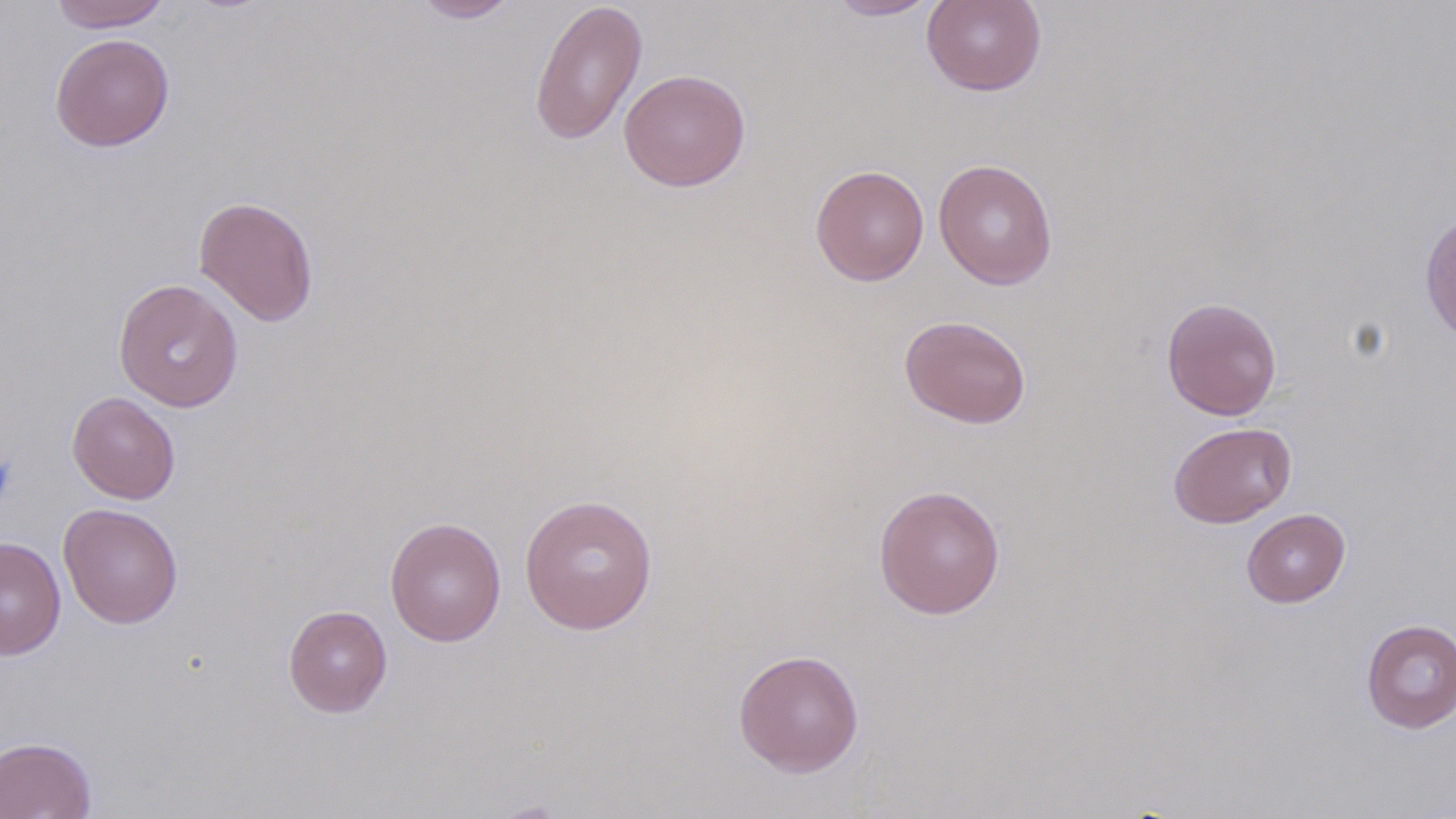 Approximate bounding boxes as [x1, y1, x2, y2] in pixels. Platelet locations: [0, 452, 18, 507]. Uninfected red blood cell locations: [49, 0, 172, 32], [409, 0, 521, 23], [824, 0, 943, 21], [921, 0, 1047, 96], [529, 1, 648, 146], [49, 33, 175, 152], [618, 68, 751, 191], [933, 158, 1058, 289], [810, 165, 930, 286], [193, 195, 320, 327], [113, 279, 244, 412], [1161, 296, 1283, 421], [899, 315, 1031, 429], [67, 392, 181, 505], [1168, 421, 1297, 528], [873, 484, 1006, 619], [520, 494, 659, 635], [58, 503, 183, 629], [1241, 508, 1351, 608], [385, 517, 507, 647], [0, 536, 66, 660], [283, 604, 393, 717], [1361, 618, 1456, 733], [733, 648, 865, 777], [0, 736, 97, 818]. Slide-level diagnosis: no evidence of blood parasites. Light microscopy. Image is 1456×819 pixels. Thin blood film. 1000x magnification. Single field of view. May-Grünwald-Giemsa-stained preparation.